Give the extent of all Plasmodium malariae-infected red blood cells.
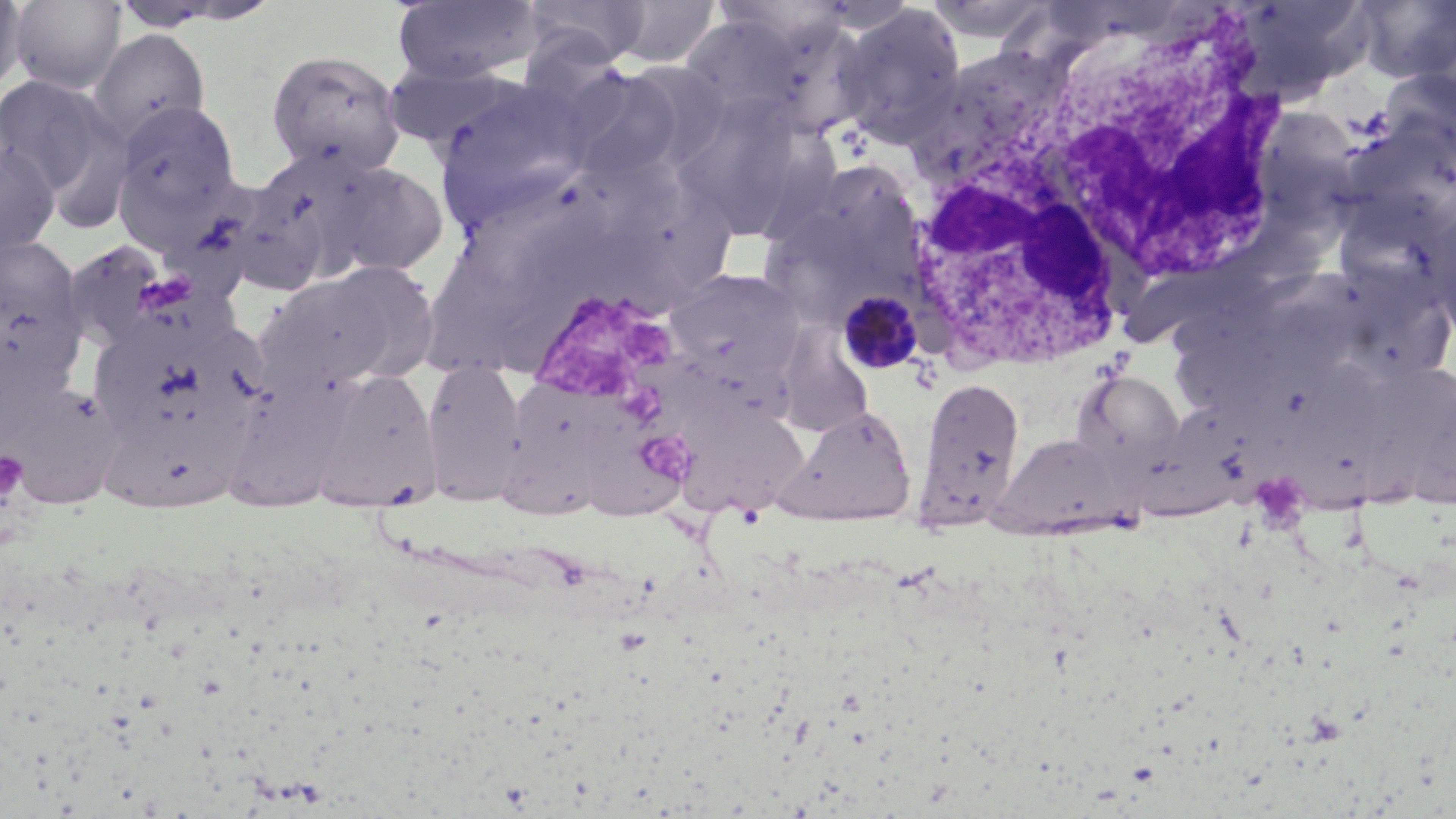
Approximate bounding boxes as named x1/y1/x2/y2 corners in pixels.
Plasmodium malariae-infected red blood cells: (x1=836, y1=289, x2=924, y2=374).

Summary:
  - Platelet locations: (x1=525, y1=287, x2=683, y2=416), (x1=0, y1=450, x2=28, y2=509)
  - Uninfected red blood cell locations: (x1=0, y1=0, x2=28, y2=98), (x1=8, y1=0, x2=128, y2=94), (x1=391, y1=0, x2=542, y2=84), (x1=519, y1=0, x2=651, y2=68), (x1=923, y1=0, x2=1057, y2=45), (x1=1227, y1=0, x2=1376, y2=101), (x1=1355, y1=0, x2=1456, y2=84), (x1=111, y1=1, x2=277, y2=32), (x1=609, y1=1, x2=719, y2=68), (x1=834, y1=3, x2=968, y2=149), (x1=678, y1=15, x2=803, y2=127), (x1=758, y1=16, x2=875, y2=141), (x1=87, y1=29, x2=212, y2=144), (x1=266, y1=48, x2=407, y2=178), (x1=381, y1=62, x2=533, y2=157), (x1=561, y1=68, x2=684, y2=182), (x1=1378, y1=72, x2=1456, y2=162), (x1=0, y1=75, x2=118, y2=198), (x1=434, y1=82, x2=593, y2=225), (x1=1256, y1=94, x2=1366, y2=225), (x1=690, y1=96, x2=800, y2=242), (x1=111, y1=100, x2=244, y2=234), (x1=0, y1=141, x2=61, y2=258), (x1=320, y1=160, x2=448, y2=279), (x1=788, y1=160, x2=924, y2=277), (x1=222, y1=179, x2=333, y2=297), (x1=0, y1=236, x2=85, y2=370), (x1=252, y1=267, x2=419, y2=395), (x1=663, y1=269, x2=803, y2=386), (x1=89, y1=307, x2=266, y2=464), (x1=773, y1=321, x2=874, y2=436), (x1=663, y1=338, x2=796, y2=440), (x1=420, y1=358, x2=528, y2=507), (x1=308, y1=368, x2=441, y2=509), (x1=1072, y1=369, x2=1183, y2=466), (x1=224, y1=371, x2=355, y2=511), (x1=507, y1=375, x2=629, y2=483), (x1=915, y1=375, x2=1025, y2=529), (x1=1, y1=383, x2=138, y2=509), (x1=1122, y1=401, x2=1259, y2=526), (x1=674, y1=402, x2=810, y2=516), (x1=774, y1=406, x2=918, y2=526), (x1=576, y1=419, x2=692, y2=521), (x1=498, y1=430, x2=606, y2=520), (x1=99, y1=432, x2=257, y2=521), (x1=993, y1=433, x2=1127, y2=537)
  - White blood cell locations: (x1=981, y1=0, x2=1295, y2=294), (x1=901, y1=142, x2=1131, y2=372)
  - Slide-level diagnosis: Plasmodium malariae
  - Modality: light microscopy
  - Magnification: 1000x
  - Stain: May-Grünwald-Giemsa
  - Field of view: single
  - Preparation: thin blood smear
  - Image size: 1456×819 pixels